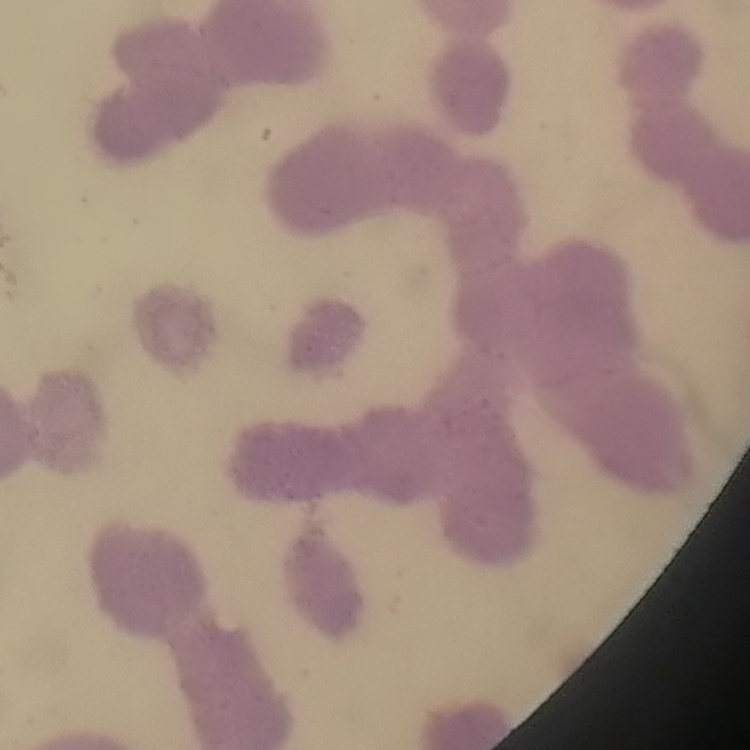
The erythrocytes exhibit rouleaux formation. Field's or Giemsa stain. Thin peripheral smear. Square crop of a larger photomicrograph.